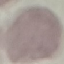
Summary:
  - Result: no malaria parasites detected
  - Capture: smartphone through the microscope eyepiece
  - Preparation: thin smear
  - Stain: Giemsa
  - Image type: automatically extracted cell patch, resized to 64 × 64 pixels